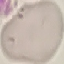
Summary:
  - Result: negative for malaria parasites
  - Image type: automatically extracted cell patch, resized to 64 × 64 pixels
  - Capture: smartphone through the microscope eyepiece
  - Stain: Giemsa
  - Preparation: thin smear